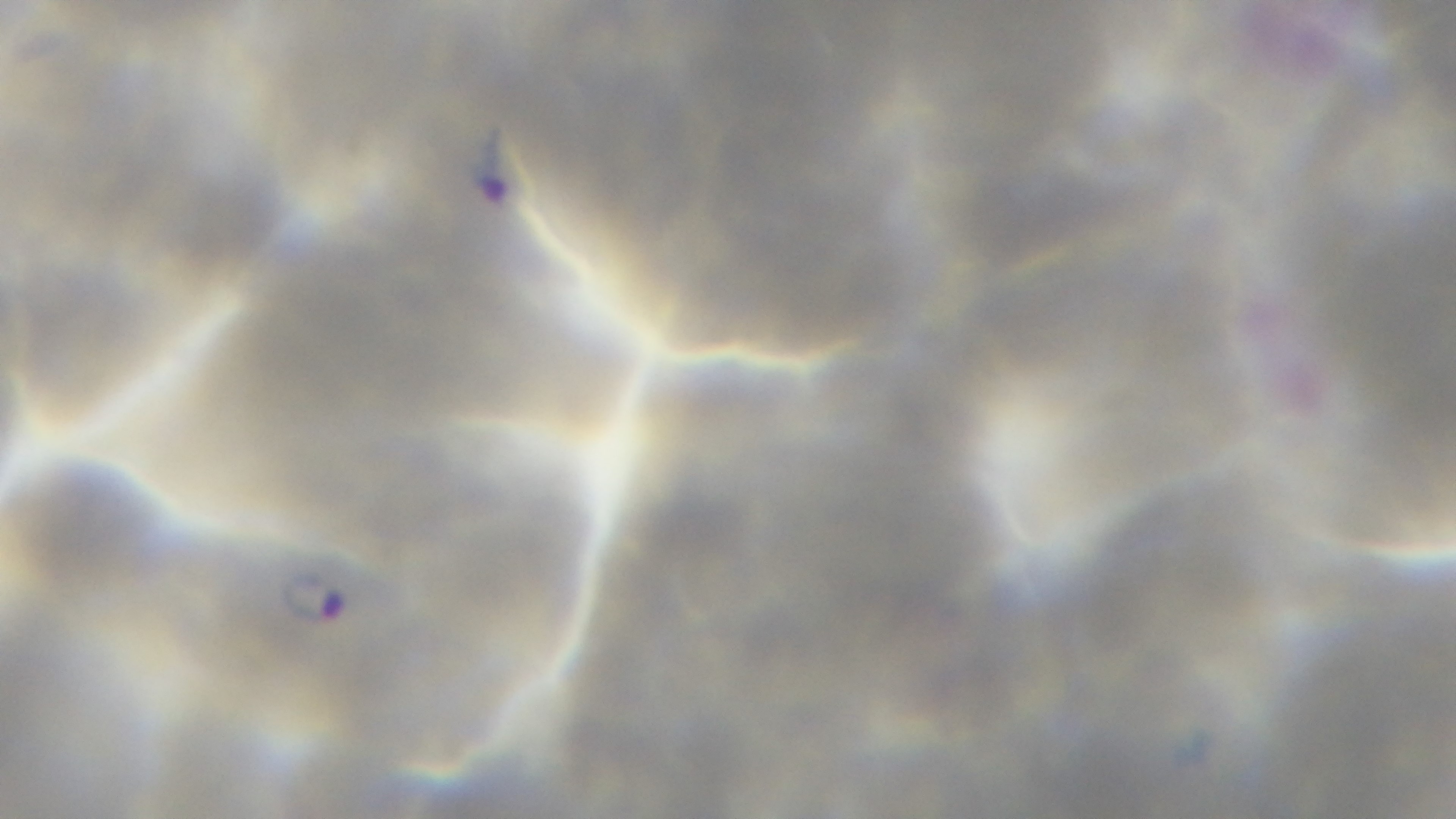
stain = Giemsa
modality = light microscopy
malaria status = infected
objective = 100x oil immersion
preparation = thin
capture = mounted 4K digital camera
field of view = one from the slide